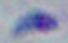
Summary:
  - Identification: Toxoplasma gondii
  - Magnification: 1000x
  - Modality: micrograph